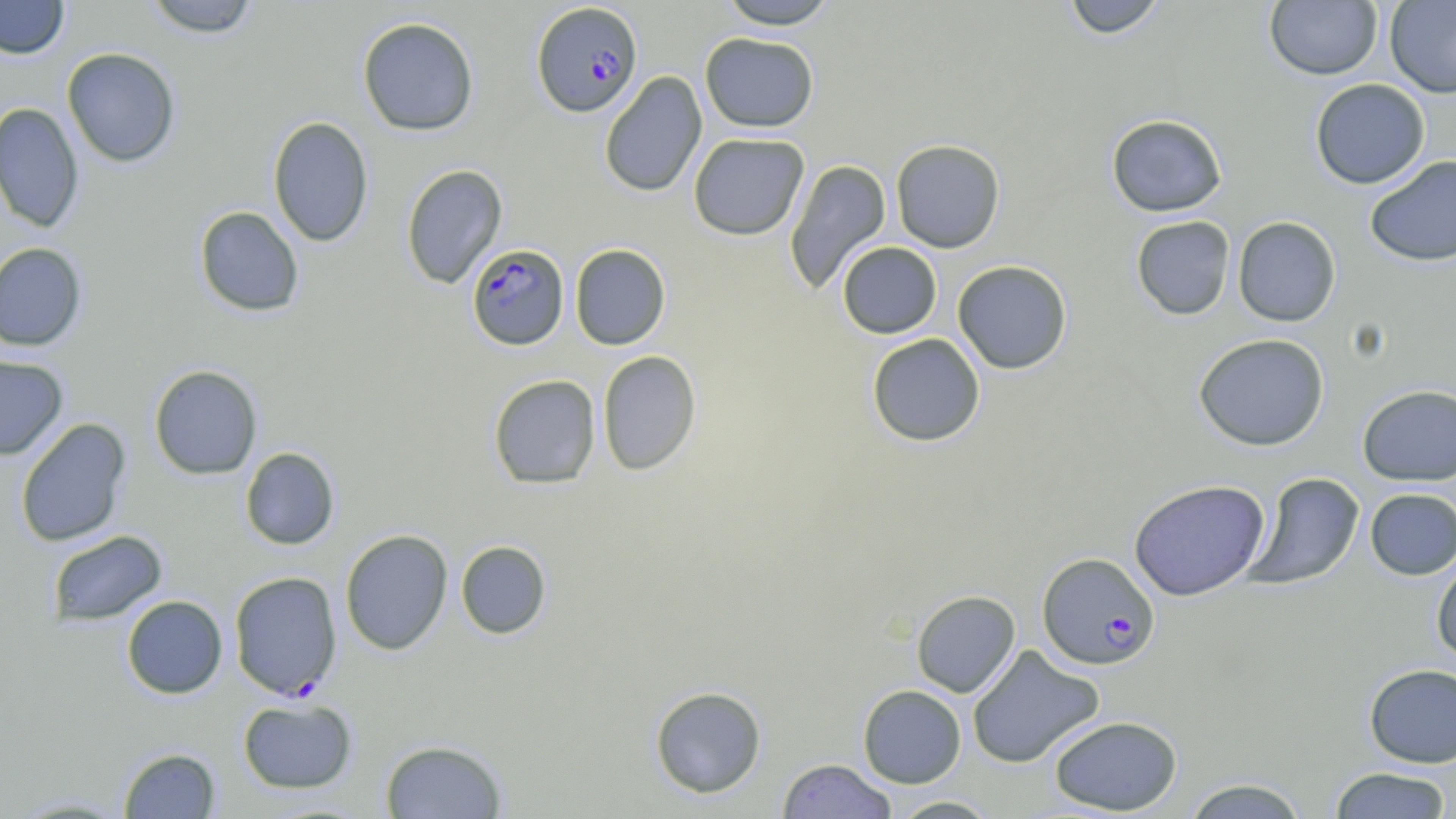
Approximate bounding boxes as (x1,y1)-(x2,y2) corner pairs in pixels. Plasmodium falciparum-infected red blood cell locations: (531,2)-(643,118), (466,243)-(569,350), (1037,552)-(1161,670), (228,570)-(342,700). Uninfected red blood cell locations: (0,0)-(69,59), (142,0)-(262,38), (716,0)-(840,30), (1061,0)-(1168,39), (1265,1)-(1382,80), (1385,1)-(1456,98), (357,16)-(480,136), (700,32)-(819,133), (62,47)-(181,167), (599,71)-(707,198), (1309,78)-(1430,189), (0,102)-(84,233), (1106,114)-(1228,217), (267,116)-(374,247), (688,133)-(809,241), (890,139)-(1006,253), (1364,155)-(1456,266), (784,159)-(891,296), (400,164)-(508,290), (194,206)-(305,317), (1131,215)-(1236,320), (1232,216)-(1342,327), (836,241)-(942,339), (0,242)-(87,351), (569,244)-(671,350), (952,260)-(1073,374), (866,333)-(985,447), (1193,333)-(1330,451), (596,350)-(701,477), (0,355)-(68,460), (148,364)-(263,480), (488,374)-(601,489), (1357,384)-(1455,486), (15,418)-(132,548), (239,447)-(340,550), (1245,472)-(1365,591), (1129,479)-(1270,601), (1364,488)-(1456,580), (340,529)-(453,655), (46,530)-(168,627), (455,540)-(552,639), (1431,555)-(1456,666), (911,590)-(1020,697), (121,595)-(228,699), (967,644)-(1105,769), (1363,663)-(1456,768), (857,684)-(966,788), (649,685)-(767,798), (237,697)-(357,793), (1048,715)-(1183,815), (380,739)-(507,818), (118,747)-(221,818), (776,759)-(898,818), (1327,767)-(1454,818), (1180,777)-(1310,818), (7,794)-(134,817), (888,795)-(1002,818). Slide-level diagnosis: Plasmodium falciparum. Captured at 1000x magnification. Thin blood film. May-Grünwald-Giemsa-stained preparation. Image is 1456×819 pixels. Single field of view. Optical microscopy.